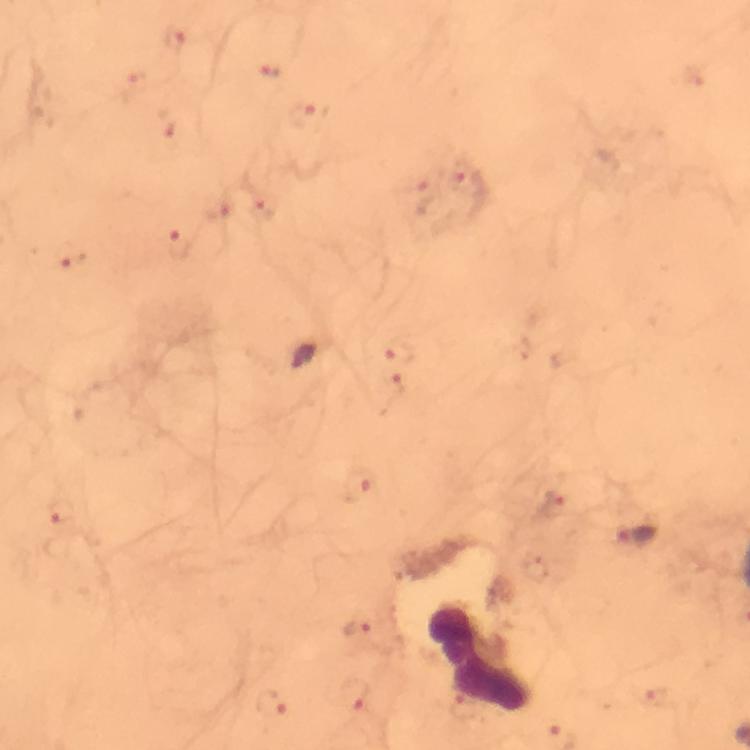

cropped_from: a single field of view
capture: smartphone photograph through a microscope
plasmodium_parasite_locations: 'approximate centers as {x, y} in pixels: {175, 37}, {269, 73}, {137, 78}, {309, 114}, {464, 178}, {428, 194}, {263, 207}, {179, 244}, {74, 260}, {400, 352}, {396, 383}, {358, 485}, {556, 507}, {62, 513}, {638, 536}, {358, 627}, {356, 696}, {273, 700}, {660, 700}'
leukocyte_locations: 'approximate centers as {x, y} in pixels: {482, 657}'
context: from a diagnostic examination for malaria
immersion_oil: applied
preparation: thick blood smear
magnification: 100x
stain: Giemsa
image_size: 750×750 pixels